Assess this cell for malaria.
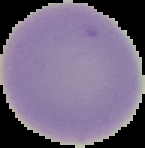

Uninfected.

{
  "image_size": "145×148 pixels",
  "preparation": "thin blood smear",
  "image_type": "segmented cell region with the area outside set to black"
}